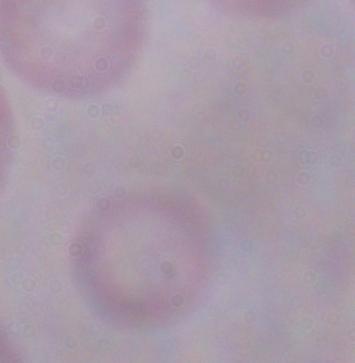
identification = trypanosome
magnification = 1000x
modality = micrograph